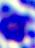
400x magnification. A white blood cell is shown. Micrograph.